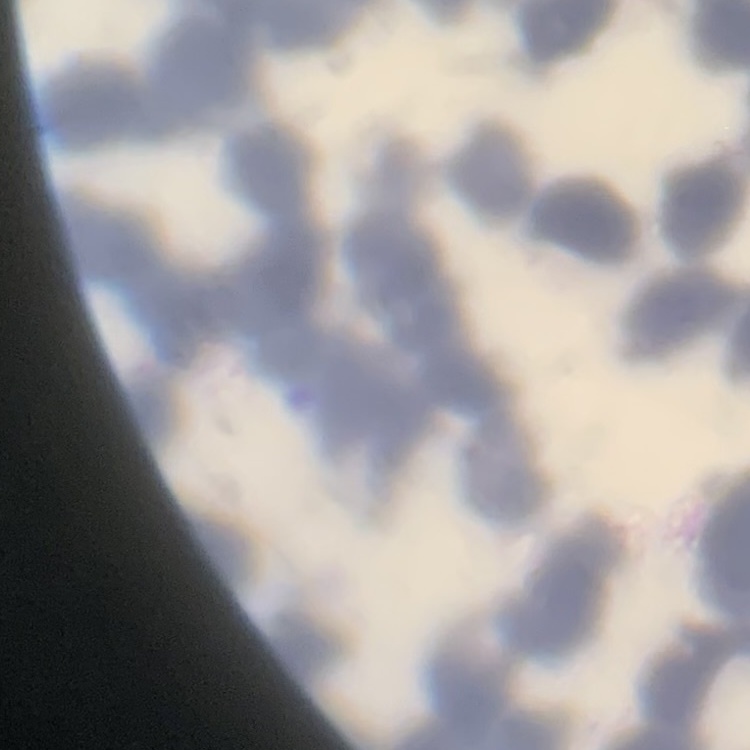

Summary:
  - Erythrocyte morphology: rouleaux formation
  - Preparation: thin peripheral smear
  - Image type: square crop of a larger photomicrograph
  - Stain: Field's or Giemsa